State the blood parasite species.
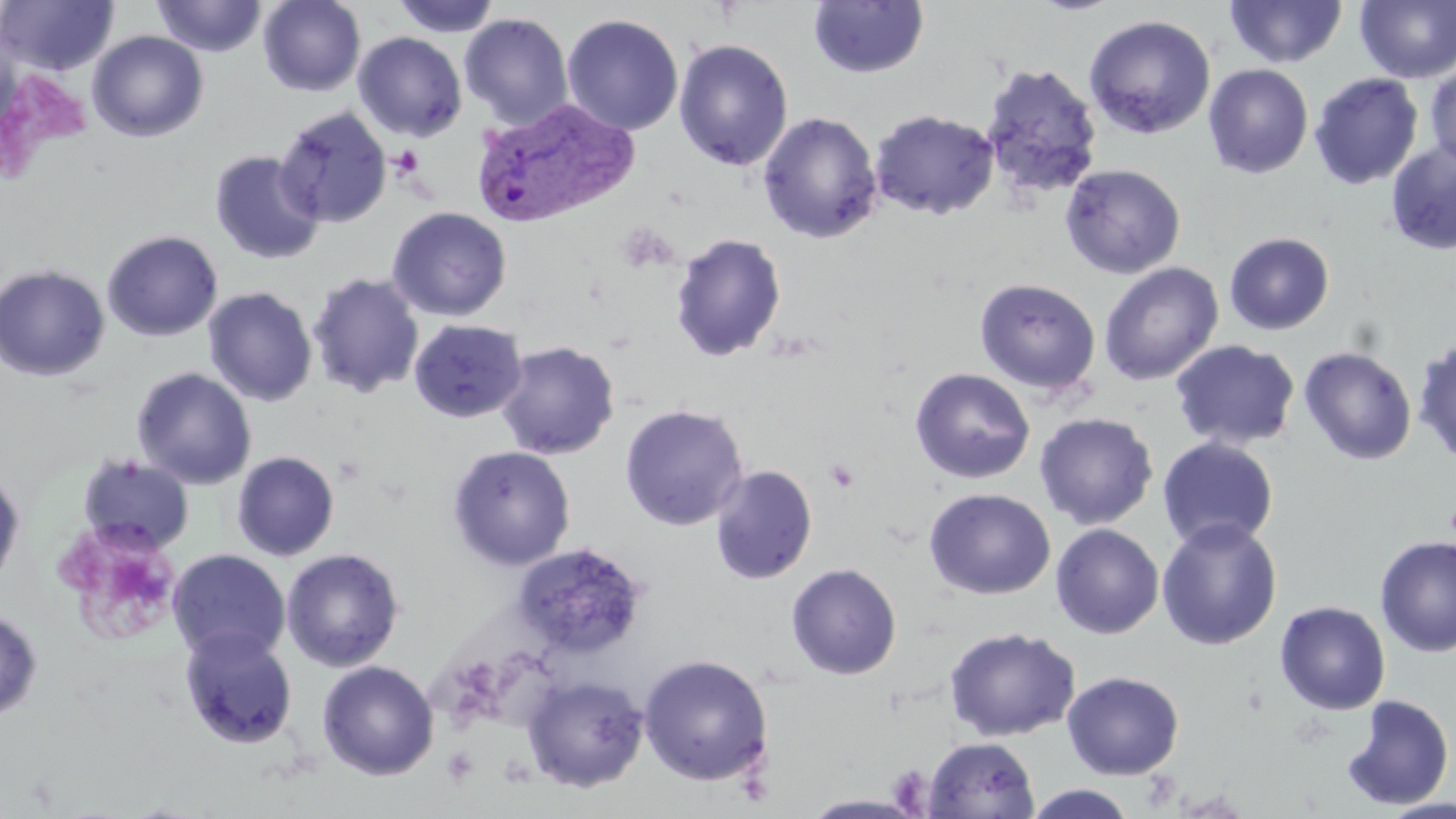
Plasmodium vivax.

stain = May-Grünwald-Giemsa
platelet locations = approximate bounding boxes as [x1, y1, x2, y2] in pixels: [389, 145, 424, 178], [825, 459, 861, 493], [56, 526, 183, 643], [443, 746, 479, 786]
field of view = one of a larger specimen
preparation = thin blood smear
modality = optical microscopy
uninfected red blood cell locations = approximate bounding boxes as [x1, y1, x2, y2] in pixels: [1, 0, 119, 76], [151, 0, 267, 57], [258, 0, 366, 96], [390, 0, 502, 38], [1225, 0, 1348, 68], [809, 1, 928, 79], [1355, 1, 1456, 83], [458, 13, 573, 129], [562, 14, 684, 136], [1083, 14, 1216, 139], [86, 30, 209, 143], [353, 32, 467, 142], [674, 39, 794, 171], [980, 63, 1103, 198], [1203, 63, 1314, 179], [1425, 64, 1456, 172], [1309, 73, 1424, 190], [274, 106, 392, 228], [869, 109, 999, 219], [757, 111, 883, 244], [1385, 140, 1456, 255], [209, 150, 325, 264], [1060, 163, 1186, 279], [387, 206, 512, 321], [101, 230, 223, 342], [670, 232, 787, 363], [1224, 232, 1334, 335], [1099, 262, 1223, 386], [0, 263, 110, 381], [307, 272, 424, 398], [974, 277, 1101, 394], [204, 287, 317, 406], [408, 319, 527, 423], [1413, 337, 1456, 466], [1170, 339, 1300, 451], [496, 341, 619, 459], [1299, 347, 1417, 465], [131, 367, 256, 489], [909, 367, 1034, 484], [620, 404, 748, 531], [1034, 412, 1158, 530], [1157, 437, 1279, 552], [447, 445, 576, 571], [231, 451, 340, 561], [78, 454, 195, 555], [710, 465, 817, 585], [0, 467, 25, 592], [923, 488, 1056, 600], [1156, 518, 1282, 651], [1051, 523, 1164, 639], [1374, 535, 1456, 658], [516, 546, 654, 665], [281, 548, 404, 672], [167, 549, 290, 664], [786, 562, 902, 680], [1275, 601, 1391, 715], [0, 607, 43, 722], [179, 627, 298, 750], [944, 627, 1081, 741], [638, 654, 774, 786], [317, 660, 439, 781], [1062, 671, 1185, 779], [521, 674, 649, 793], [1340, 694, 1455, 810], [923, 736, 1040, 819], [1023, 784, 1140, 819], [802, 794, 926, 818], [1378, 798, 1456, 819]
magnification = 1000x
image size = 1456×819 pixels
Plasmodium vivax-infected red blood cell locations = approximate bounding boxes as [x1, y1, x2, y2] in pixels: [472, 94, 639, 226]